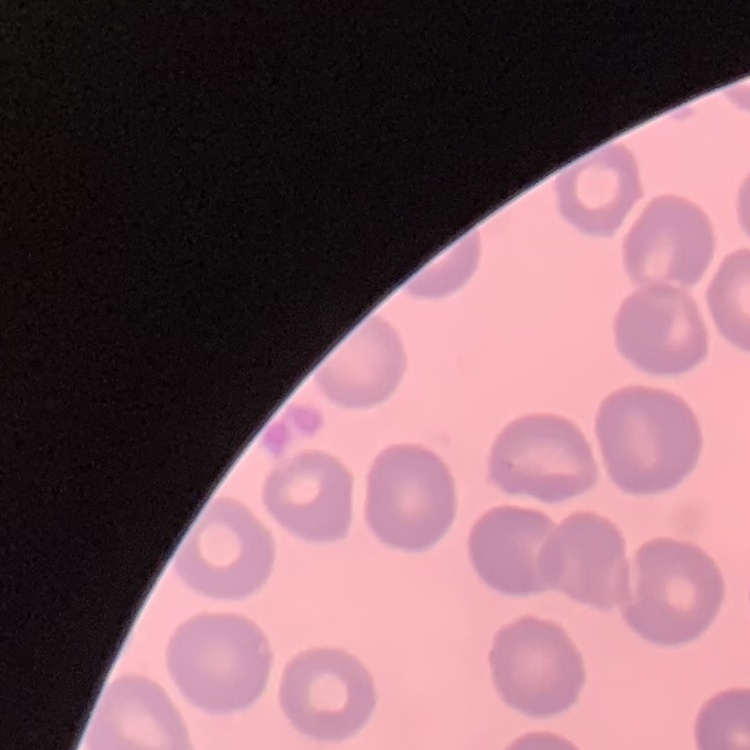
erythrocyte morphology = no rouleaux formation
preparation = thin blood film
image type = square crop of a larger photomicrograph
stain = Field's or Giemsa